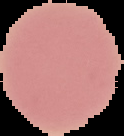

From a thin blood smear. Malaria status: uninfected. Segmented cell region on a black background. Image is 124×136 pixels.